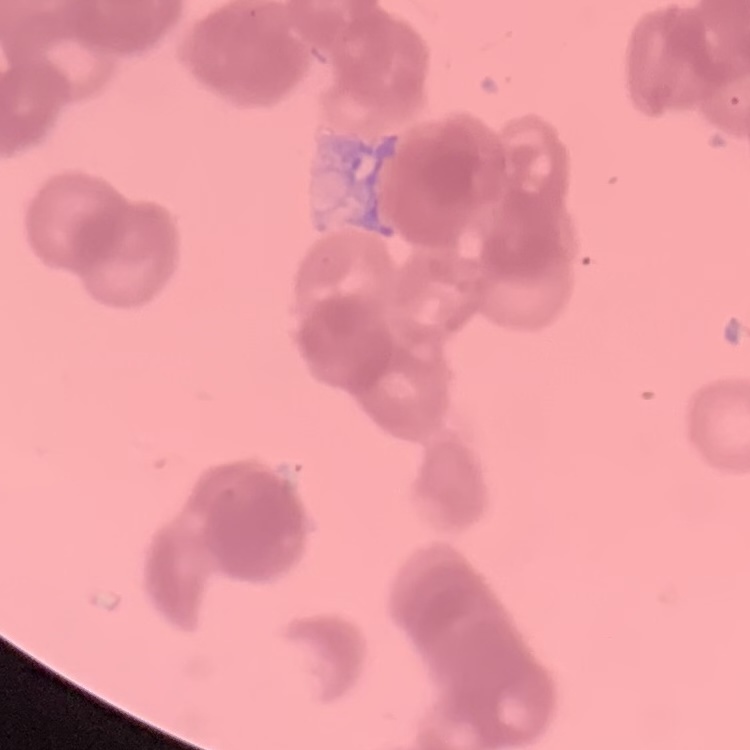

Summary:
  - Erythrocyte morphology: rouleaux formation
  - Preparation: thin blood film
  - Stain: Field's or Giemsa
  - Image type: one tile cut from a larger photomicrograph